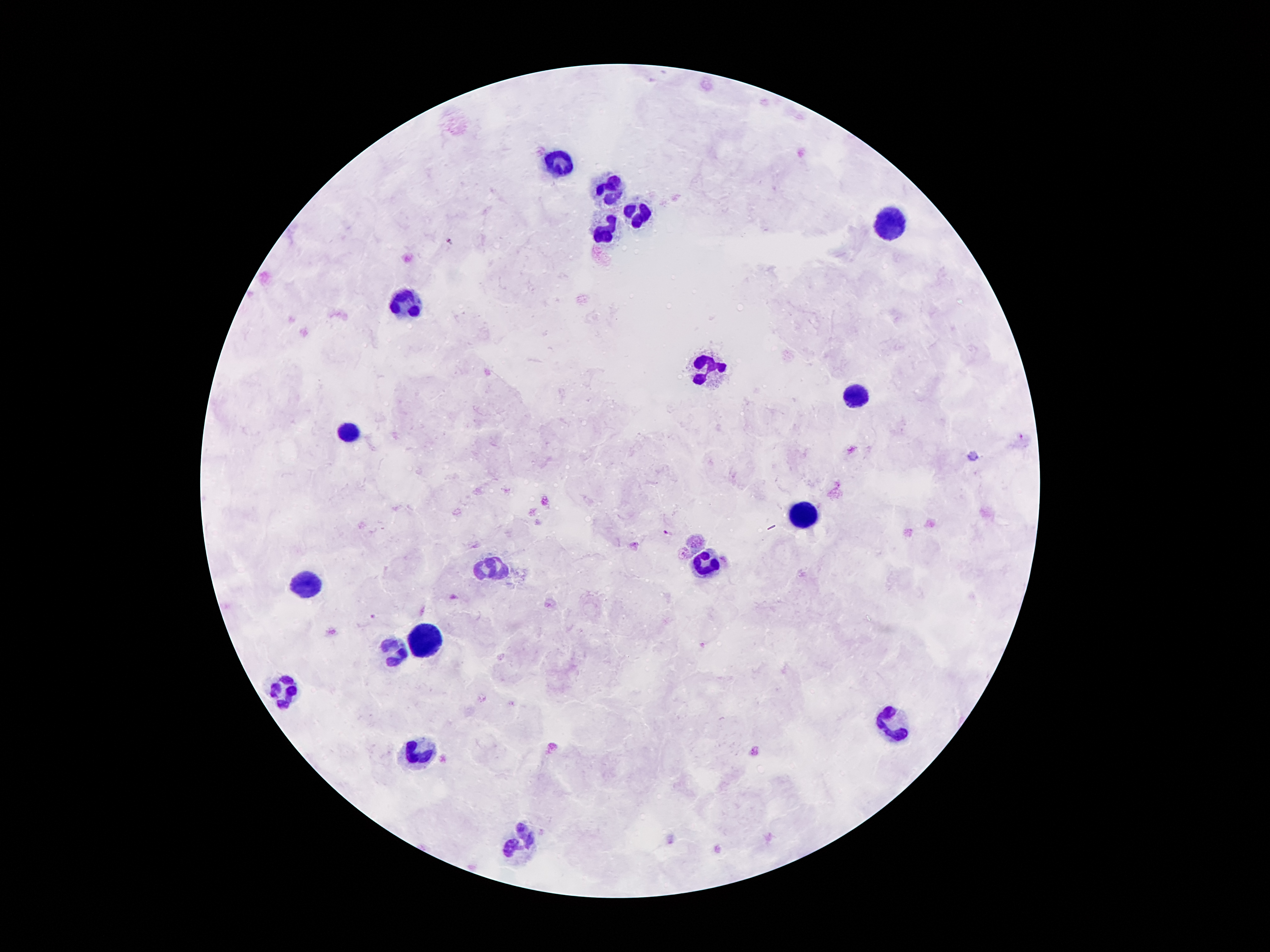

coordinate format = approximate object centers, in pixels from the top-left corner
Plasmodium parasite locations = (x=452, y=241), (x=668, y=534), (x=374, y=616)
leukocyte locations = (x=562, y=166), (x=609, y=193), (x=636, y=217), (x=888, y=223), (x=605, y=234), (x=410, y=307), (x=702, y=370), (x=855, y=394), (x=351, y=435), (x=802, y=517), (x=704, y=568), (x=492, y=570), (x=306, y=589), (x=425, y=641), (x=398, y=651), (x=285, y=690), (x=890, y=729), (x=419, y=754), (x=521, y=839)
patient malaria status = positive for Plasmodium falciparum
field of view = single
preparation = thick blood film
capture = smartphone through the microscope eyepiece
image size = 1270×952 pixels
stain = Giemsa
magnification = 100x